Report the malaria status of this cell.
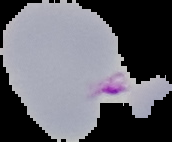

It is parasitized.

Summary:
  - Image type: segmented cell region with the area outside set to black
  - Image size: 172×142 pixels
  - Preparation: thin blood smear